Evaluate for malaria.
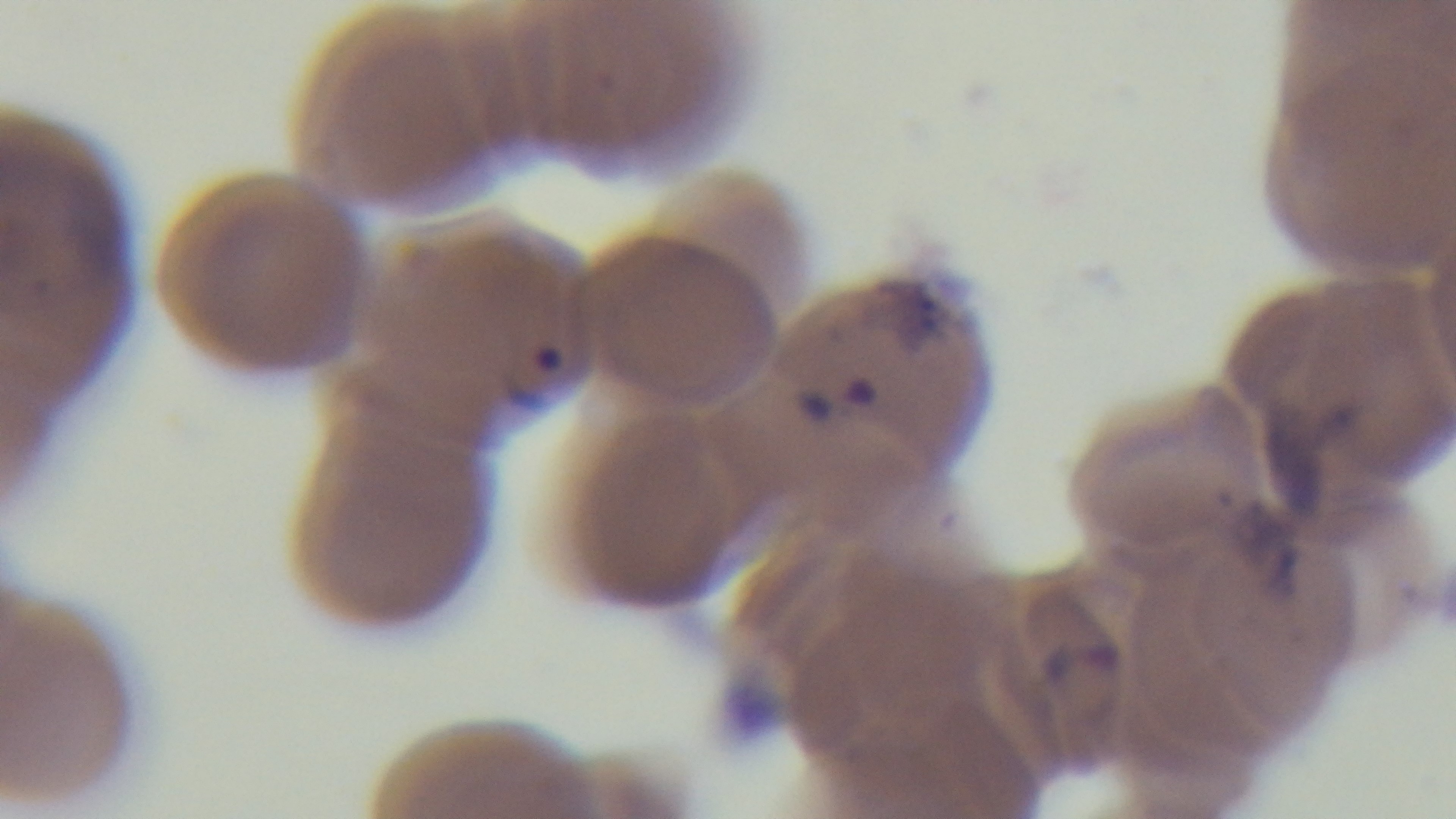

Infected.

Summary:
  - Preparation: thin smear
  - Stain: Giemsa
  - Field of view: one from the slide
  - Objective: 100x oil immersion
  - Capture: mounted 4K digital camera
  - Modality: light microscopy